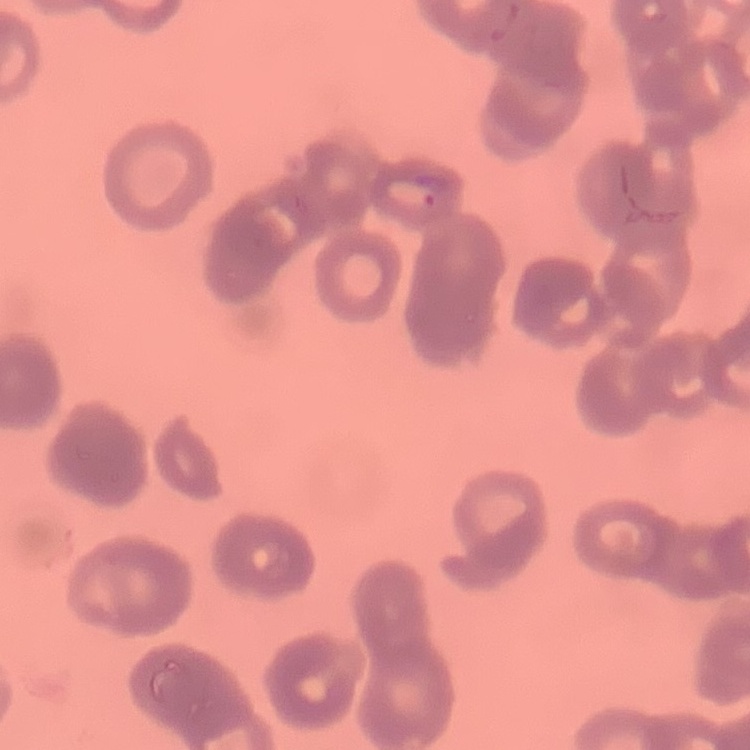
The red blood cells exhibit rouleaux formation. Field's or Giemsa stain. Thin blood smear. Square crop of a larger photomicrograph.